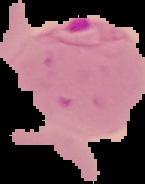

image type = cell region segmented out of the field of view; surrounding area masked to black
malaria status = parasitized
preparation = thin blood film
image size = 145×184 pixels